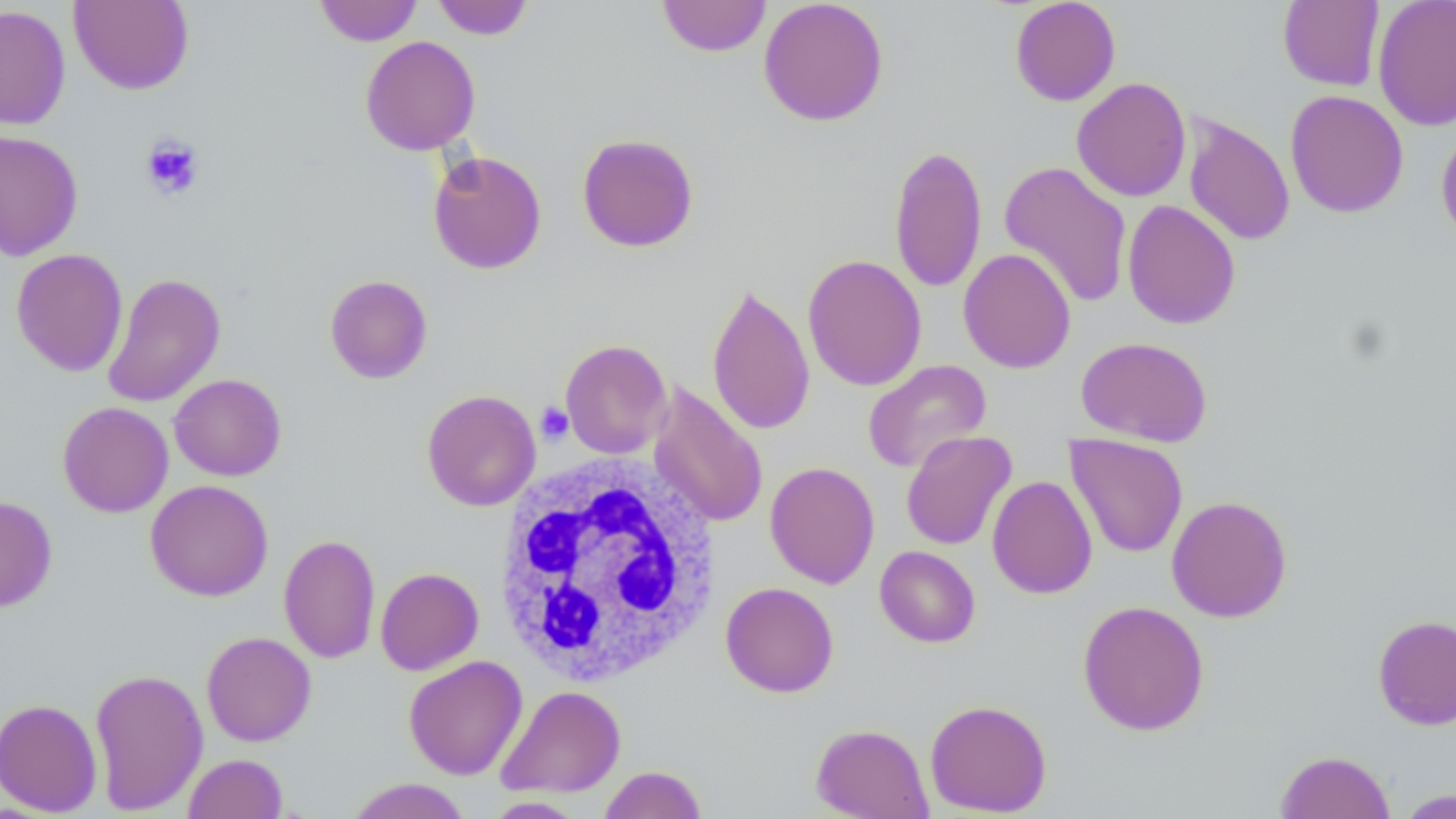
Approximate bounding boxes as named x1/y1/x2/y2 corners in pixels. White blood cell locations: (x1=494, y1=455, x2=722, y2=687). Uninfected red blood cell locations: (x1=314, y1=0, x2=422, y2=46), (x1=431, y1=0, x2=534, y2=40), (x1=657, y1=0, x2=771, y2=57), (x1=758, y1=0, x2=889, y2=126), (x1=1009, y1=0, x2=1121, y2=106), (x1=1372, y1=0, x2=1456, y2=132), (x1=69, y1=1, x2=194, y2=95), (x1=1278, y1=1, x2=1384, y2=91), (x1=0, y1=5, x2=71, y2=130), (x1=360, y1=35, x2=481, y2=155), (x1=1071, y1=77, x2=1192, y2=202), (x1=1285, y1=89, x2=1409, y2=218), (x1=1183, y1=114, x2=1295, y2=246), (x1=1435, y1=126, x2=1456, y2=248), (x1=0, y1=129, x2=84, y2=261), (x1=576, y1=133, x2=699, y2=252), (x1=889, y1=144, x2=987, y2=293), (x1=428, y1=150, x2=547, y2=274), (x1=999, y1=160, x2=1133, y2=309), (x1=1122, y1=199, x2=1241, y2=330), (x1=11, y1=248, x2=128, y2=377), (x1=958, y1=248, x2=1076, y2=373), (x1=802, y1=254, x2=927, y2=391), (x1=102, y1=273, x2=226, y2=408), (x1=324, y1=274, x2=433, y2=384), (x1=706, y1=281, x2=815, y2=436), (x1=1076, y1=336, x2=1213, y2=447), (x1=559, y1=339, x2=672, y2=459), (x1=863, y1=359, x2=992, y2=474), (x1=169, y1=373, x2=287, y2=481), (x1=648, y1=383, x2=769, y2=529), (x1=422, y1=389, x2=541, y2=512), (x1=57, y1=401, x2=173, y2=517), (x1=901, y1=430, x2=1017, y2=551), (x1=1065, y1=434, x2=1188, y2=558), (x1=765, y1=461, x2=880, y2=589), (x1=987, y1=475, x2=1098, y2=599), (x1=145, y1=479, x2=273, y2=601), (x1=1167, y1=495, x2=1292, y2=622), (x1=0, y1=496, x2=58, y2=613), (x1=278, y1=534, x2=381, y2=664), (x1=874, y1=546, x2=980, y2=647), (x1=276, y1=554, x2=481, y2=668), (x1=375, y1=567, x2=483, y2=675), (x1=720, y1=582, x2=839, y2=698), (x1=1077, y1=600, x2=1209, y2=736), (x1=1372, y1=614, x2=1456, y2=730), (x1=201, y1=631, x2=316, y2=746), (x1=404, y1=655, x2=527, y2=780), (x1=89, y1=667, x2=208, y2=814), (x1=496, y1=685, x2=626, y2=798), (x1=0, y1=697, x2=103, y2=816), (x1=925, y1=698, x2=1052, y2=816), (x1=810, y1=723, x2=933, y2=818), (x1=1275, y1=750, x2=1396, y2=819), (x1=183, y1=753, x2=288, y2=819), (x1=599, y1=765, x2=708, y2=819), (x1=344, y1=778, x2=473, y2=819), (x1=1395, y1=789, x2=1456, y2=818), (x1=483, y1=796, x2=587, y2=818). Platelet locations: (x1=141, y1=134, x2=205, y2=200), (x1=536, y1=402, x2=574, y2=444). Slide-level diagnosis: no evidence of blood parasites. Thin blood smear. Light microscopy. May-Grünwald-Giemsa-stained preparation. One field of a larger specimen. Image is 1456×819 pixels. Captured at 1000x magnification.